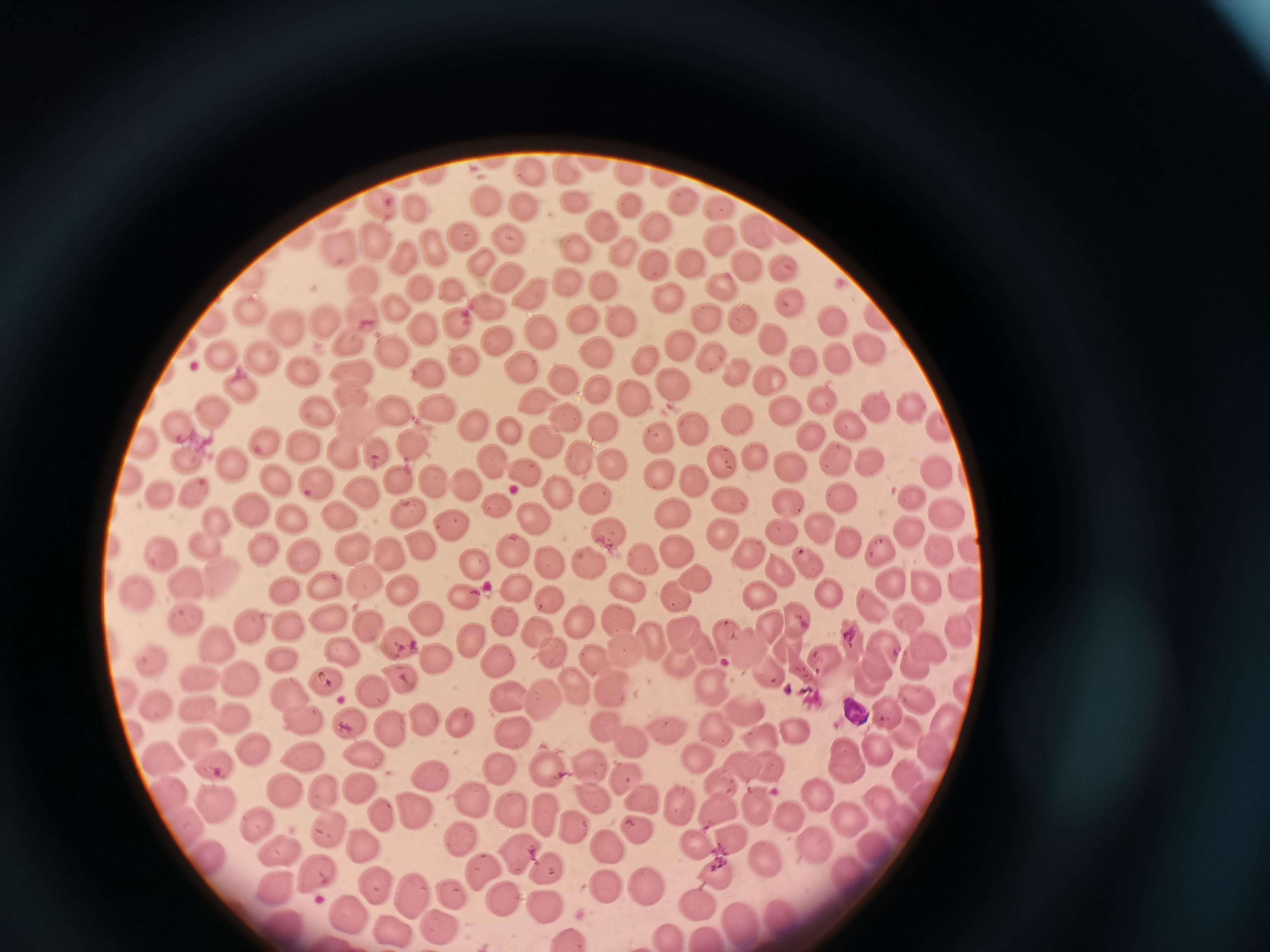
cell locations = approximate centers as [x, y] in pixels: [527, 168], [561, 170], [483, 197], [577, 202], [678, 202], [522, 203], [626, 205], [411, 207], [716, 208], [601, 225], [655, 228], [756, 232], [460, 239], [511, 240], [724, 241], [379, 243], [432, 245], [572, 248], [336, 250], [619, 253], [407, 255], [484, 258], [693, 261], [653, 264], [745, 267], [781, 268], [502, 276], [367, 278], [567, 283], [603, 283], [720, 287], [419, 288], [453, 290], [527, 293], [666, 297], [488, 301], [787, 302], [250, 309], [399, 309], [362, 312], [322, 315], [707, 316], [584, 317], [459, 319], [624, 321], [744, 321], [833, 321], [287, 324], [422, 327], [539, 335], [770, 338], [352, 340], [495, 341], [676, 345], [396, 346], [867, 346], [595, 351], [218, 354], [643, 355], [709, 356], [259, 359], [803, 360], [836, 361], [463, 363], [515, 363], [353, 370], [734, 370], [430, 375], [302, 377], [766, 377], [561, 378], [672, 382], [595, 387], [240, 388], [352, 392], [631, 392], [817, 394], [534, 402], [872, 403], [395, 405], [207, 406], [911, 407], [781, 409], [435, 411], [568, 413], [316, 414], [738, 418], [355, 420], [842, 424], [179, 425], [940, 425], [603, 426], [691, 427], [471, 429], [511, 429], [804, 434], [658, 436], [413, 438], [142, 439], [263, 440], [545, 442], [304, 448], [347, 449], [376, 449], [755, 454], [586, 457], [835, 457], [191, 463], [233, 463], [491, 463], [721, 463], [789, 466], [867, 466], [612, 467], [933, 469], [662, 473], [524, 474], [276, 475], [397, 479], [695, 479], [436, 480], [463, 484], [321, 485], [559, 488], [362, 490], [158, 492], [915, 492], [190, 495], [594, 496], [728, 497], [838, 497], [787, 500], [498, 503], [248, 505], [670, 508], [406, 509], [944, 510], [337, 513], [293, 517], [535, 518], [217, 519], [450, 523], [909, 526], [817, 528], [608, 530], [781, 530], [719, 532], [415, 542], [849, 542], [203, 543], [262, 545], [676, 546], [880, 547], [512, 548], [939, 548], [970, 548], [300, 550], [353, 550], [160, 551], [388, 551], [749, 551], [649, 557], [808, 560], [550, 561], [476, 563], [589, 563], [775, 567], [222, 578], [697, 578], [889, 578], [364, 580], [186, 582], [926, 582], [963, 582], [327, 583], [627, 586], [401, 587], [515, 588], [287, 589], [681, 591], [830, 591], [758, 592], [139, 594], [462, 597], [549, 598], [872, 604], [326, 612], [423, 614], [577, 616], [615, 616], [795, 617], [908, 617], [185, 620], [364, 621], [507, 621], [251, 622], [292, 625], [765, 625], [538, 630], [956, 630], [678, 631], [470, 636], [724, 636], [651, 637], [848, 637], [216, 640], [394, 641], [789, 643], [931, 644], [742, 646], [551, 647], [623, 647], [345, 649], [591, 655], [887, 655], [286, 657], [822, 657], [150, 658], [495, 658], [433, 659], [677, 659], [915, 663], [764, 671], [326, 676], [197, 677], [401, 677], [869, 678], [240, 683], [575, 683], [712, 685], [374, 686], [609, 687], [966, 689], [123, 693], [288, 693], [508, 695], [544, 697], [913, 700], [159, 704], [192, 708], [742, 711], [882, 714], [231, 716], [302, 716], [421, 716], [459, 718], [347, 719], [948, 721], [604, 722], [665, 727], [715, 728], [903, 728], [391, 729], [793, 729], [511, 735], [758, 736], [198, 738], [633, 738], [249, 748], [929, 749], [304, 752], [165, 754], [697, 754], [365, 755], [845, 758], [585, 762], [741, 762], [219, 765], [495, 765], [767, 767], [545, 770], [426, 774], [623, 774], [901, 774], [721, 782], [362, 787], [286, 788], [327, 789], [168, 792], [592, 793], [816, 793], [639, 796], [873, 796], [470, 799], [218, 802], [679, 804], [757, 805], [416, 806], [510, 807], [716, 807], [785, 811], [549, 812], [842, 816], [382, 819], [330, 822], [253, 823], [574, 825], [179, 827], [633, 828], [460, 833], [363, 842], [694, 842], [728, 842], [811, 844], [612, 845], [278, 852], [514, 854], [767, 856], [208, 859], [485, 868], [549, 868], [715, 870], [316, 873], [855, 873], [373, 880], [277, 884], [602, 884], [642, 887], [410, 892], [453, 893], [503, 896], [698, 898], [545, 901], [349, 912], [782, 916], [739, 917], [280, 922], [435, 922], [393, 925], [668, 934], [707, 935], [570, 937]
image size = 1270×952 pixels
capture = smartphone camera at the microscope eyepiece
stain = Giemsa
field of view = single
preparation = thin blood film